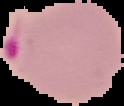
Summary:
  - Image type: segmented cell region with the area outside set to black
  - Result: Plasmodium parasites identified
  - Image size: 124×106 pixels
  - Preparation: thin blood film